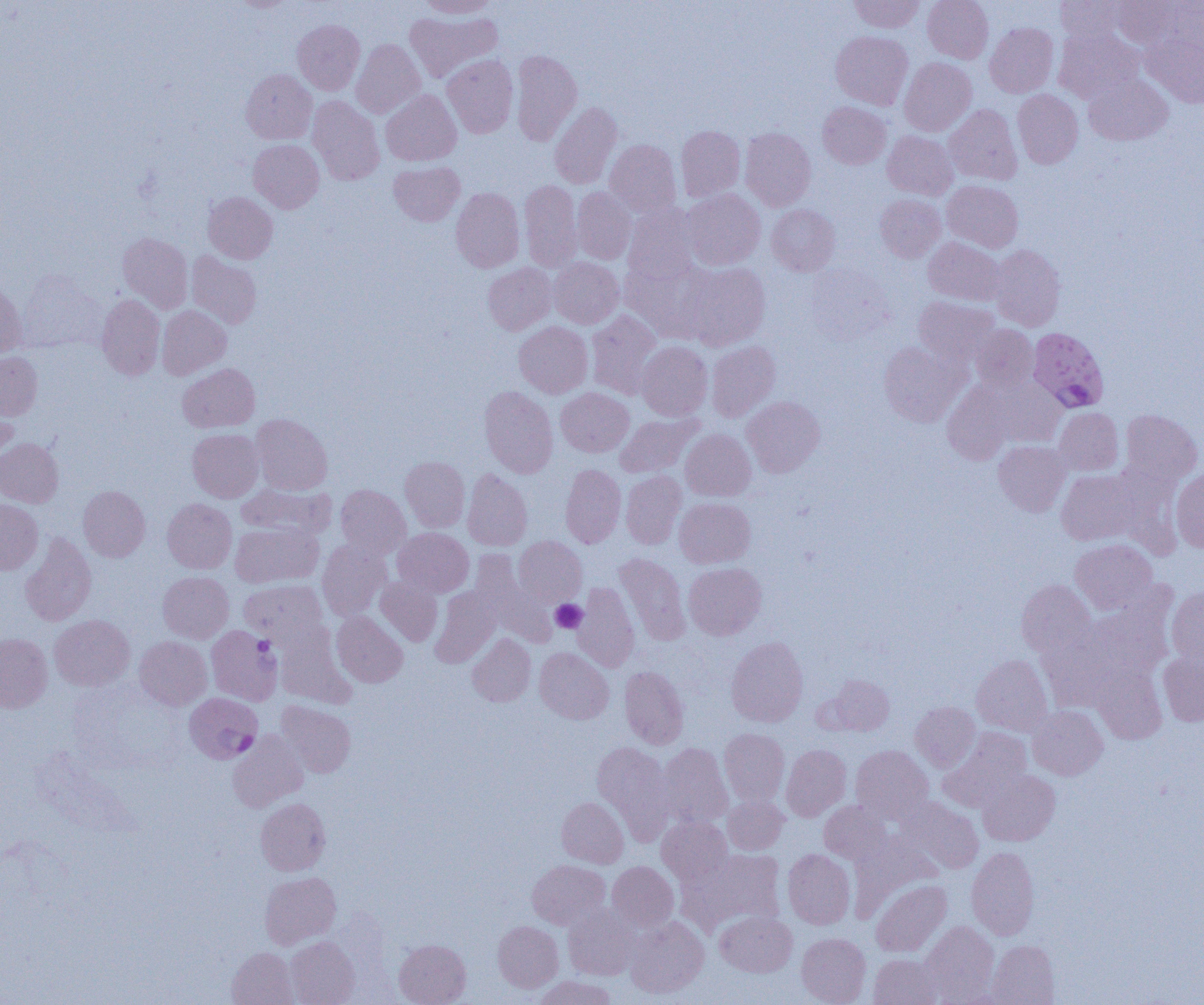 Approximate bounding boxes as (x1, y1, x2, y2) in pixels. Uninfected red blood cell locations: (417, 0, 499, 18), (850, 0, 924, 32), (923, 0, 993, 63), (1056, 0, 1125, 43), (1108, 0, 1183, 48), (1154, 1, 1204, 59), (404, 10, 501, 82), (293, 19, 365, 95), (985, 22, 1058, 97), (1055, 28, 1143, 103), (831, 31, 912, 109), (1143, 32, 1204, 107), (351, 39, 425, 119), (511, 50, 582, 146), (442, 54, 518, 138), (900, 58, 976, 136), (241, 69, 317, 144), (1084, 73, 1172, 145), (381, 89, 461, 166), (1013, 90, 1083, 168), (307, 96, 384, 184), (550, 102, 622, 189), (818, 102, 891, 168), (943, 104, 1022, 184), (676, 126, 745, 202), (740, 128, 815, 211), (882, 131, 957, 200), (248, 139, 324, 213), (604, 140, 682, 218), (389, 161, 464, 226), (942, 180, 1023, 253), (520, 181, 582, 272), (451, 187, 524, 272), (573, 187, 636, 264), (682, 188, 764, 270), (203, 192, 278, 263), (875, 194, 946, 262), (623, 204, 701, 282), (766, 204, 840, 275), (117, 232, 193, 313), (923, 237, 1006, 306), (989, 245, 1066, 331), (187, 251, 261, 329), (549, 258, 623, 328), (621, 258, 711, 342), (680, 262, 771, 350), (483, 263, 557, 335), (806, 264, 892, 343), (17, 272, 105, 352), (0, 280, 25, 356), (97, 293, 165, 380), (914, 296, 1000, 366), (157, 305, 231, 379), (587, 310, 661, 399), (514, 322, 592, 398), (970, 324, 1038, 390), (707, 341, 780, 421), (636, 342, 712, 420), (879, 342, 966, 426), (0, 352, 42, 420), (178, 363, 259, 432), (987, 377, 1067, 447), (942, 383, 1015, 463), (480, 386, 558, 478), (556, 387, 633, 456), (741, 397, 825, 476), (0, 401, 18, 469), (1053, 407, 1123, 475), (1120, 409, 1202, 485), (615, 413, 703, 478), (251, 414, 332, 495), (187, 428, 263, 502), (680, 429, 755, 501), (0, 437, 64, 507), (994, 441, 1070, 516), (400, 456, 469, 531), (560, 464, 625, 548), (462, 469, 532, 551), (1171, 469, 1204, 552), (1056, 470, 1140, 545), (621, 471, 686, 549), (335, 484, 411, 559), (237, 485, 334, 541), (78, 486, 150, 562), (674, 497, 755, 568), (162, 498, 236, 573), (0, 499, 43, 574), (230, 521, 322, 587), (393, 527, 474, 597), (20, 533, 96, 626), (514, 536, 586, 606), (1070, 539, 1157, 613), (317, 540, 391, 621), (470, 549, 555, 645), (615, 553, 690, 643), (684, 562, 766, 639), (158, 571, 233, 643), (376, 576, 442, 646), (240, 580, 327, 645), (1016, 580, 1095, 658), (572, 583, 640, 672), (430, 587, 500, 667), (1167, 587, 1204, 664), (1078, 605, 1174, 683), (332, 612, 407, 687), (50, 615, 134, 691), (1039, 624, 1128, 710), (276, 631, 354, 708), (0, 634, 52, 713), (468, 634, 535, 706), (134, 636, 212, 710), (726, 637, 808, 726), (535, 647, 614, 724), (1158, 651, 1204, 726), (972, 655, 1052, 736), (1091, 664, 1167, 744), (620, 666, 689, 749), (830, 674, 894, 735), (276, 701, 356, 777), (910, 701, 980, 771), (1027, 705, 1108, 780), (720, 728, 789, 806), (941, 729, 1031, 809), (228, 731, 308, 811), (592, 741, 676, 844), (657, 743, 732, 828), (781, 744, 851, 821), (851, 745, 933, 821), (978, 770, 1060, 846), (723, 795, 789, 855), (557, 797, 628, 868), (898, 797, 983, 874), (256, 798, 330, 875), (819, 801, 892, 865), (657, 816, 732, 885), (966, 846, 1039, 940), (683, 848, 786, 934), (783, 849, 855, 929), (528, 860, 610, 929), (607, 861, 678, 932), (260, 872, 341, 949), (871, 880, 951, 956), (563, 905, 638, 980), (715, 910, 797, 977), (625, 916, 709, 998), (493, 921, 563, 991), (921, 921, 999, 1002), (796, 933, 871, 1005), (286, 936, 359, 1005), (394, 939, 471, 1005), (988, 940, 1060, 1005), (227, 948, 298, 1005), (869, 954, 944, 1004), (535, 976, 617, 1005). Plasmodium falciparum-infected red blood cell locations: (1027, 327, 1109, 412), (206, 626, 282, 705), (184, 692, 262, 764). Platelet locations: (551, 599, 587, 633). Slide-level diagnosis: Plasmodium falciparum. Image is 1204×1005 pixels. Thin blood smear. Optical microscopy. One field of a larger specimen. 1000x magnification.